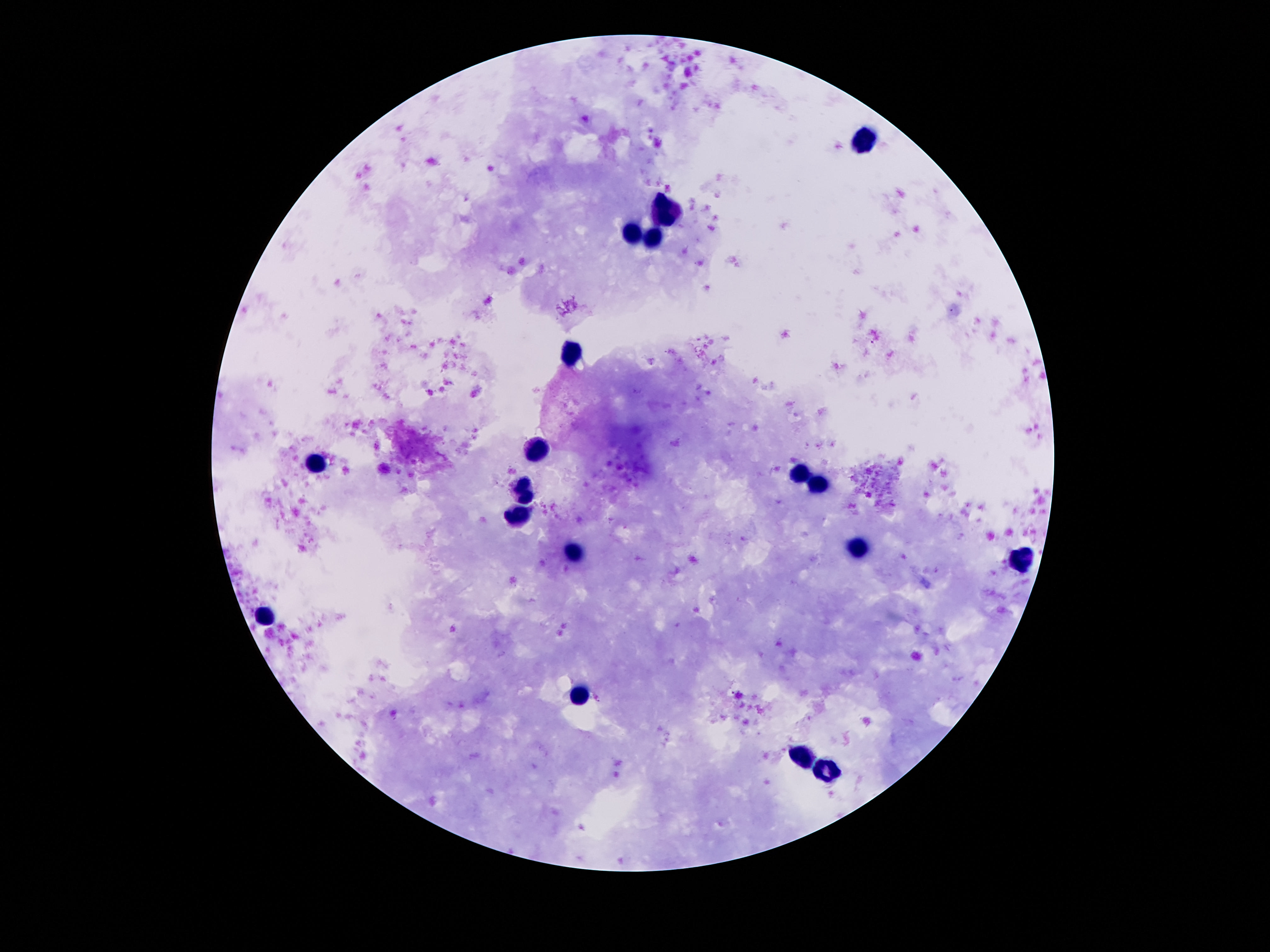

image size = 1270×952 pixels
preparation = thick blood film
patient malaria status = negative
capture = smartphone camera through the microscope eyepiece
stain = Giemsa
magnification = 100x
leukocyte locations = approximate centers as [x, y] in pixels: [865, 141], [667, 212], [631, 234], [654, 239], [572, 355], [540, 449], [314, 464], [798, 475], [818, 484], [525, 490], [519, 514], [854, 548], [570, 553], [1020, 562], [265, 615], [579, 698], [803, 757], [827, 774]
field of view = single